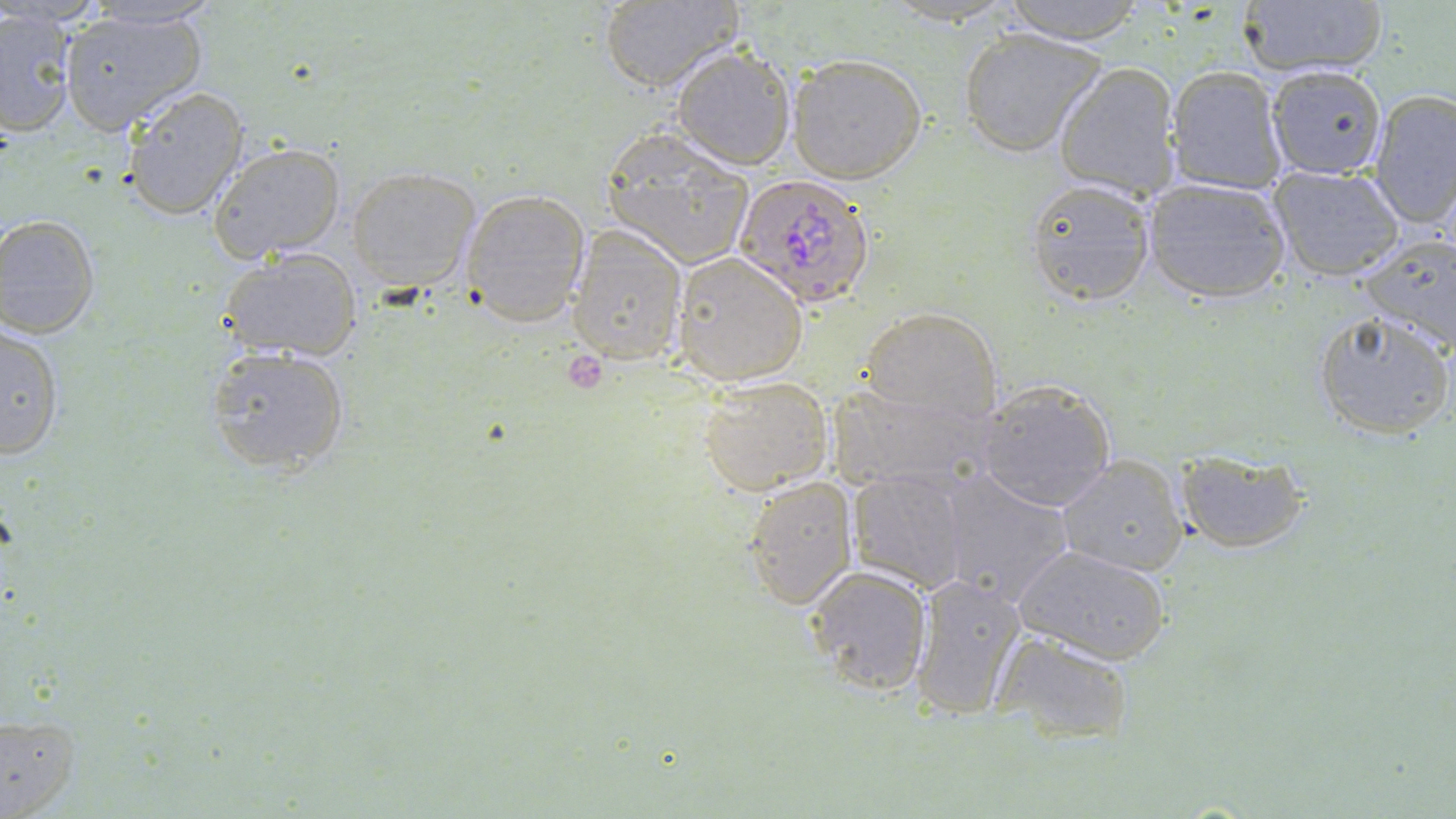
Approximate bounding boxes as (x1, y1, x2, y2) in pixels. Platelet locations: (559, 351, 610, 394). Uninfected red blood cell locations: (78, 0, 225, 28), (998, 0, 1147, 44), (1236, 0, 1388, 80), (599, 1, 742, 92), (879, 1, 1018, 29), (0, 8, 78, 136), (57, 8, 209, 134), (958, 28, 1107, 158), (671, 44, 796, 170), (787, 54, 926, 184), (1052, 62, 1180, 201), (1266, 63, 1389, 179), (1165, 65, 1287, 196), (120, 86, 249, 222), (1367, 89, 1456, 230), (600, 130, 756, 270), (207, 141, 348, 262), (1268, 164, 1408, 281), (346, 166, 482, 289), (1142, 176, 1291, 304), (1024, 177, 1156, 305), (460, 188, 590, 326), (0, 214, 100, 338), (566, 224, 688, 367), (1356, 235, 1456, 355), (219, 248, 363, 360), (673, 252, 807, 385), (862, 307, 1003, 424), (1314, 309, 1454, 439), (1, 323, 64, 463), (204, 345, 351, 477), (697, 375, 835, 496), (827, 379, 995, 494), (973, 380, 1117, 512), (1176, 446, 1312, 552), (1056, 455, 1189, 575), (847, 466, 973, 593), (936, 469, 1076, 607), (743, 473, 860, 608), (1011, 543, 1172, 664), (802, 564, 934, 699), (909, 575, 1029, 719), (990, 631, 1136, 744), (0, 712, 79, 816). Plasmodium falciparum-infected red blood cell locations: (735, 172, 877, 307). Slide-level diagnosis: Plasmodium falciparum. Thin blood smear. Light microscopy. Single field of view. May-Grünwald-Giemsa-stained preparation. Captured at 1000x magnification. Image is 1456×819 pixels.